Outline each blood parasite and name the species.
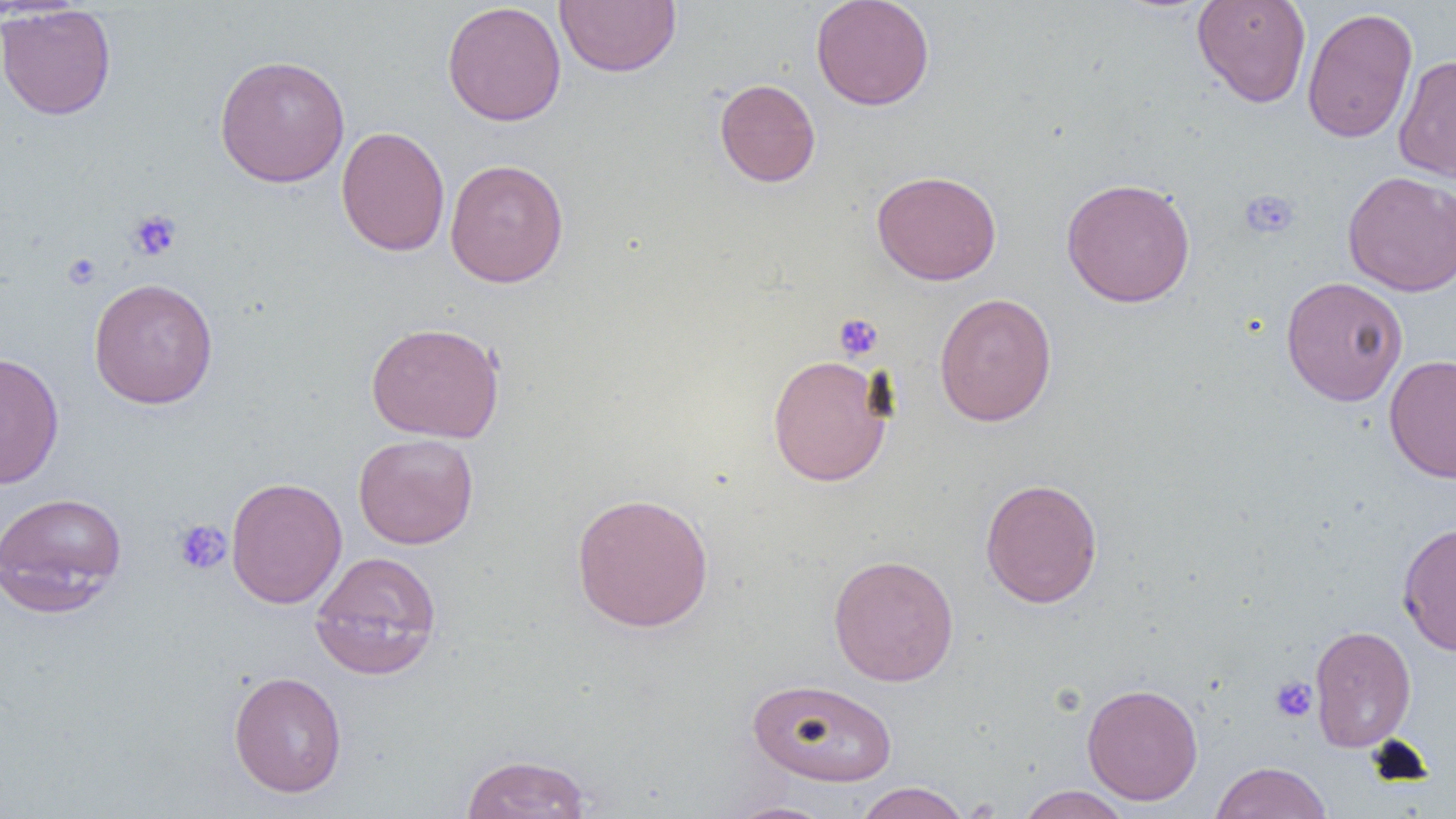
No blood parasites seen.

slide-level diagnosis = negative for blood parasites
uninfected red blood cell locations = approximate bounding boxes as named x1/y1/x2/y2 corners in pixels: (x1=810, y1=0, x2=935, y2=111), (x1=1191, y1=0, x2=1312, y2=108), (x1=555, y1=1, x2=681, y2=77), (x1=442, y1=2, x2=567, y2=127), (x1=0, y1=4, x2=117, y2=120), (x1=1301, y1=7, x2=1418, y2=144), (x1=213, y1=54, x2=350, y2=187), (x1=1393, y1=54, x2=1456, y2=183), (x1=714, y1=78, x2=821, y2=187), (x1=335, y1=126, x2=450, y2=257), (x1=444, y1=158, x2=569, y2=288), (x1=871, y1=169, x2=1001, y2=285), (x1=1342, y1=170, x2=1456, y2=296), (x1=1060, y1=177, x2=1196, y2=308), (x1=1280, y1=276, x2=1408, y2=406), (x1=88, y1=277, x2=219, y2=409), (x1=934, y1=293, x2=1057, y2=426), (x1=365, y1=321, x2=505, y2=443), (x1=0, y1=350, x2=64, y2=489), (x1=767, y1=354, x2=893, y2=487), (x1=1384, y1=354, x2=1456, y2=483), (x1=353, y1=433, x2=479, y2=550), (x1=226, y1=476, x2=347, y2=609), (x1=980, y1=477, x2=1104, y2=608), (x1=0, y1=491, x2=127, y2=612), (x1=571, y1=492, x2=714, y2=632), (x1=1397, y1=521, x2=1456, y2=656), (x1=309, y1=549, x2=443, y2=680), (x1=828, y1=553, x2=959, y2=687), (x1=1309, y1=624, x2=1416, y2=753), (x1=228, y1=671, x2=348, y2=798), (x1=747, y1=678, x2=898, y2=787), (x1=1081, y1=682, x2=1203, y2=805), (x1=460, y1=753, x2=593, y2=819), (x1=1209, y1=761, x2=1333, y2=819), (x1=852, y1=782, x2=971, y2=819), (x1=1015, y1=785, x2=1132, y2=818), (x1=723, y1=800, x2=838, y2=819)
preparation = thin blood smear
magnification = 1000x
field of view = single
platelet locations = approximate bounding boxes as named x1/y1/x2/y2 corners in pixels: (x1=1239, y1=189, x2=1300, y2=239), (x1=127, y1=209, x2=183, y2=261), (x1=62, y1=252, x2=102, y2=289), (x1=834, y1=313, x2=884, y2=361), (x1=172, y1=519, x2=232, y2=575), (x1=1270, y1=676, x2=1317, y2=723)
image size = 1456×819 pixels
modality = optical microscopy